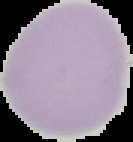

Result: no Plasmodium parasites seen. Image is 133×142 pixels. Segmented cell region on a black background. From a thin blood smear.